Point out each Plasmodium parasite.
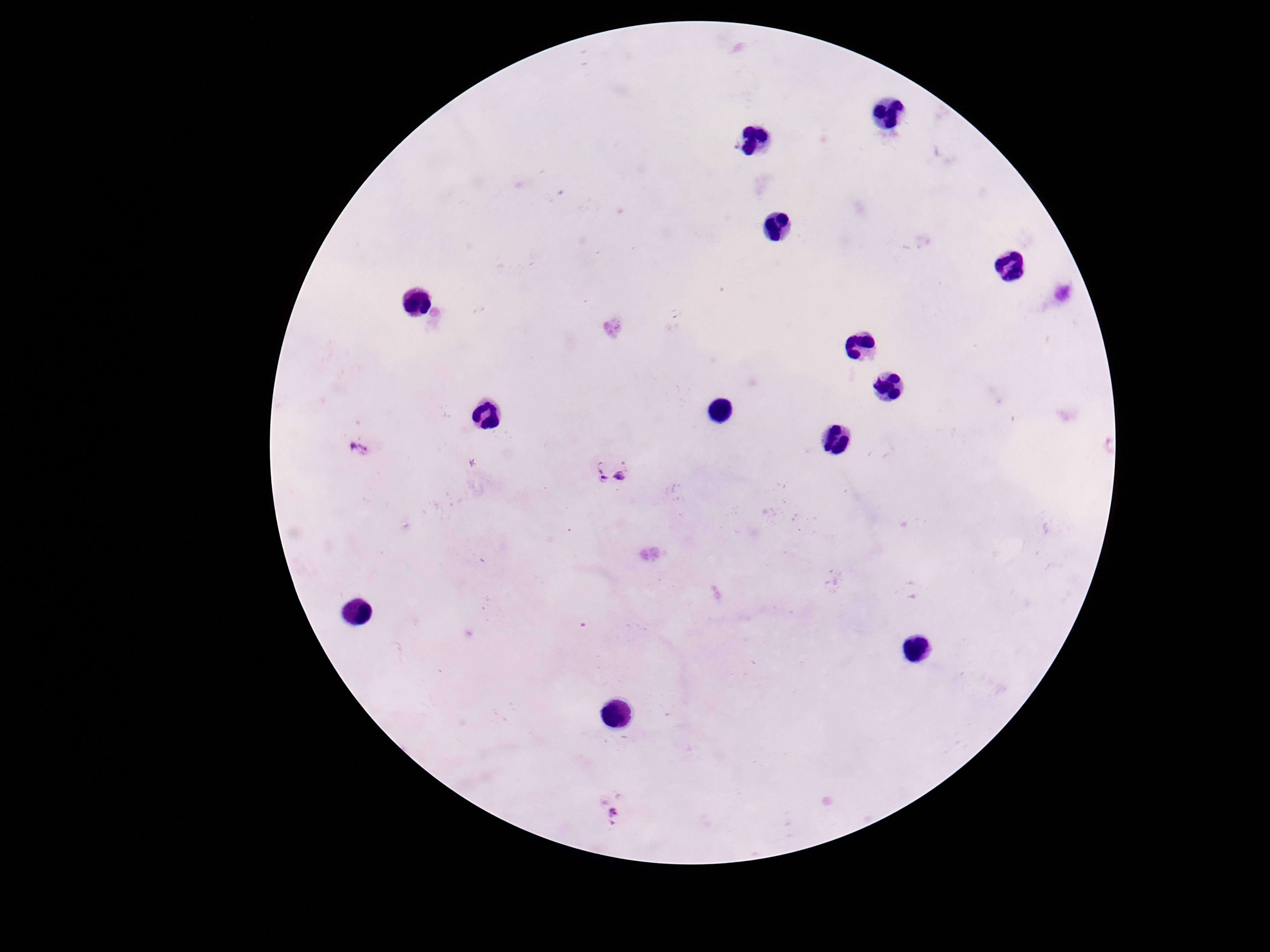

Approximate centers as [x, y] in pixels.
Plasmodium parasites: [360, 447], [614, 470], [618, 813].

One field from this slide. Photographed through the microscope eyepiece with a smartphone camera. Image is 1270×952 pixels. Thick peripheral-blood smear. 100x magnification. Giemsa-stained preparation. Patient malaria status: infected.